Give the preparation type.
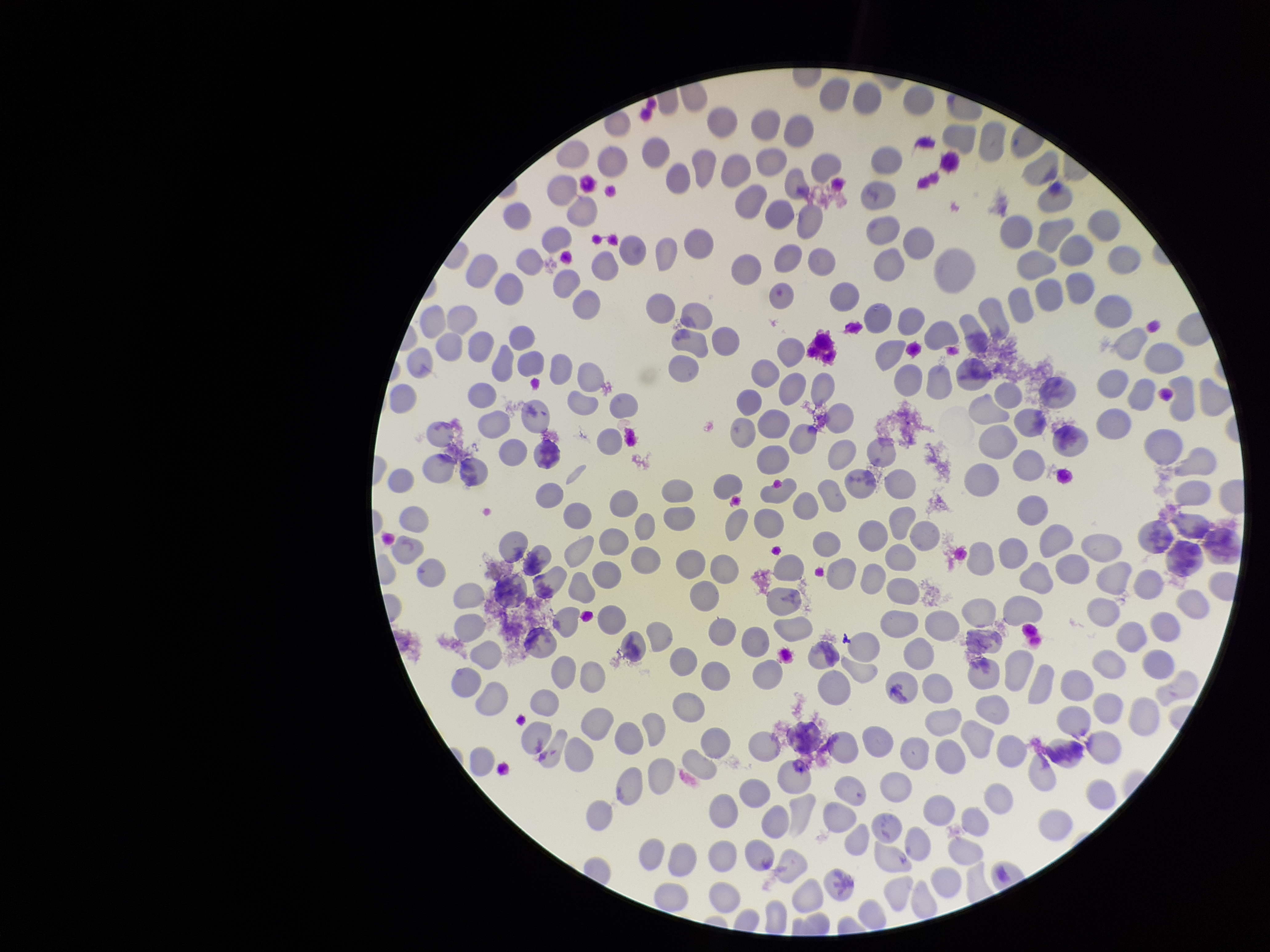
Thin.

Single field of view. Parasitized red blood cell count: 0. Patient malaria status: negative. Smartphone photograph taken through the eyepiece of a microscope. Parasitized red blood cells: none detected. Image is 1270×952 pixels. Red blood cell count: 266. Stained with Giemsa.